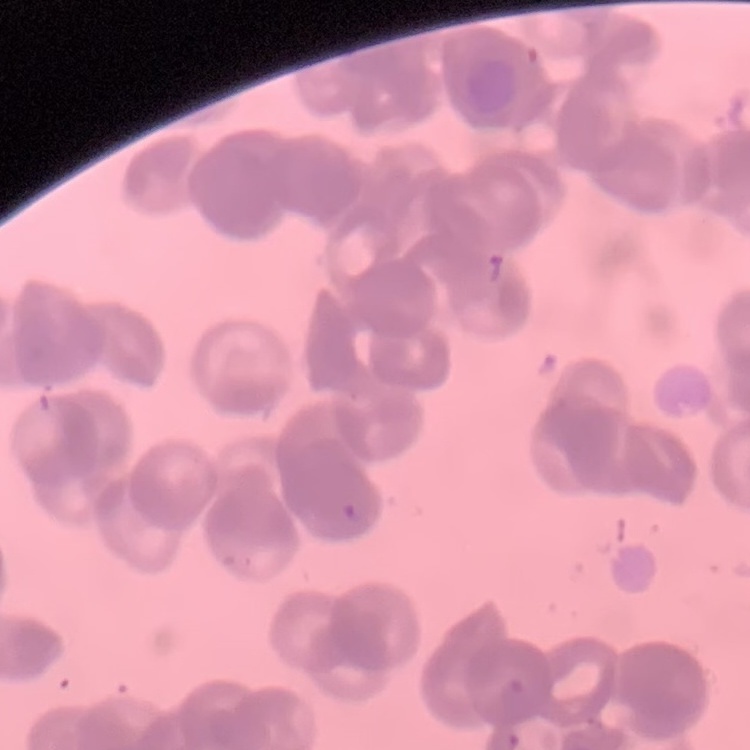
Summary:
  - Red blood cell morphology: rouleaux formation
  - Preparation: thin peripheral smear
  - Image type: one tile cut from a larger photomicrograph
  - Stain: Field's or Giemsa